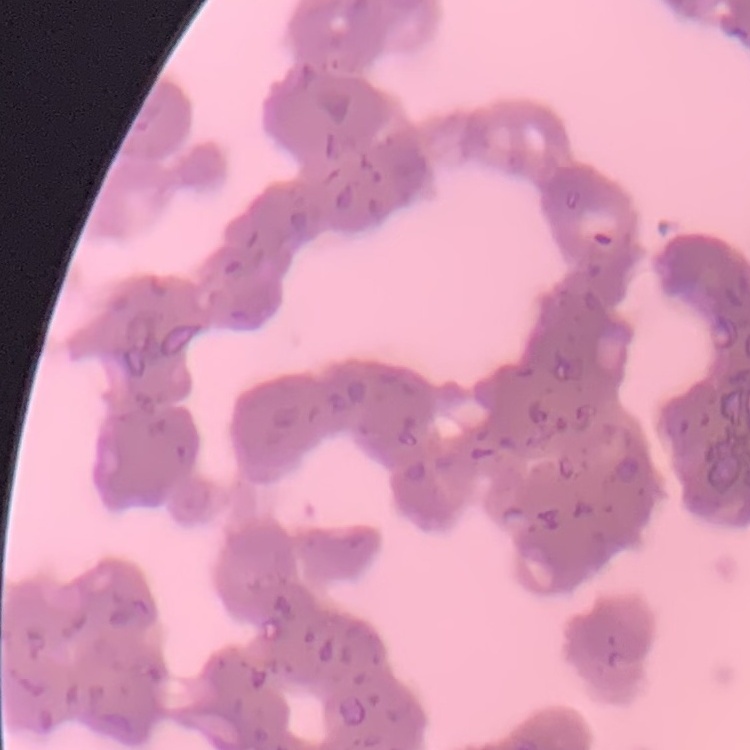
erythrocyte morphology = rouleaux formation
stain = Field's or Giemsa
preparation = thin peripheral smear
image type = square crop of a larger photomicrograph